Comment on the morphology of the erythrocytes.
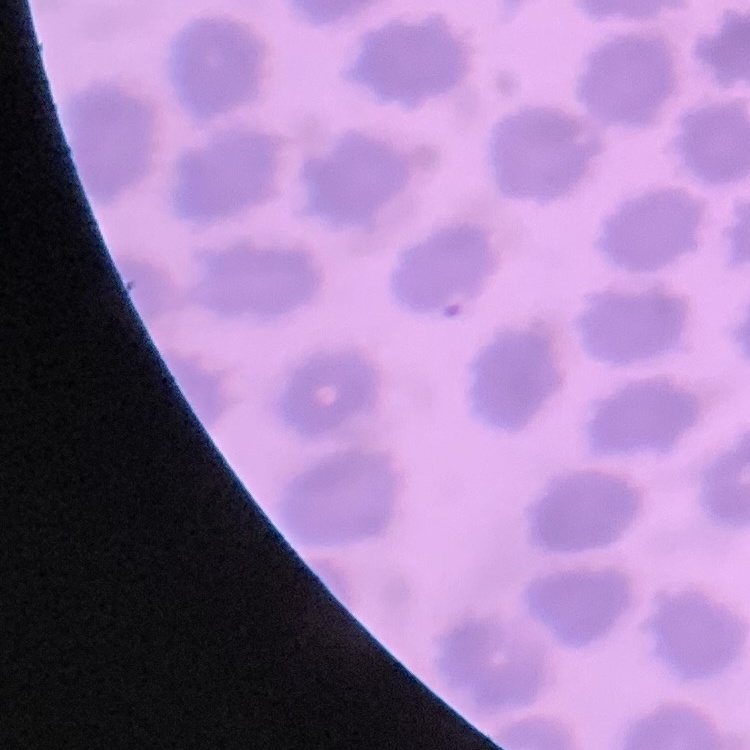

They show no rouleaux formation.

stain = Field's or Giemsa
preparation = thin blood smear
image type = square crop of a larger photomicrograph